Assess for Plasmodium parasites.
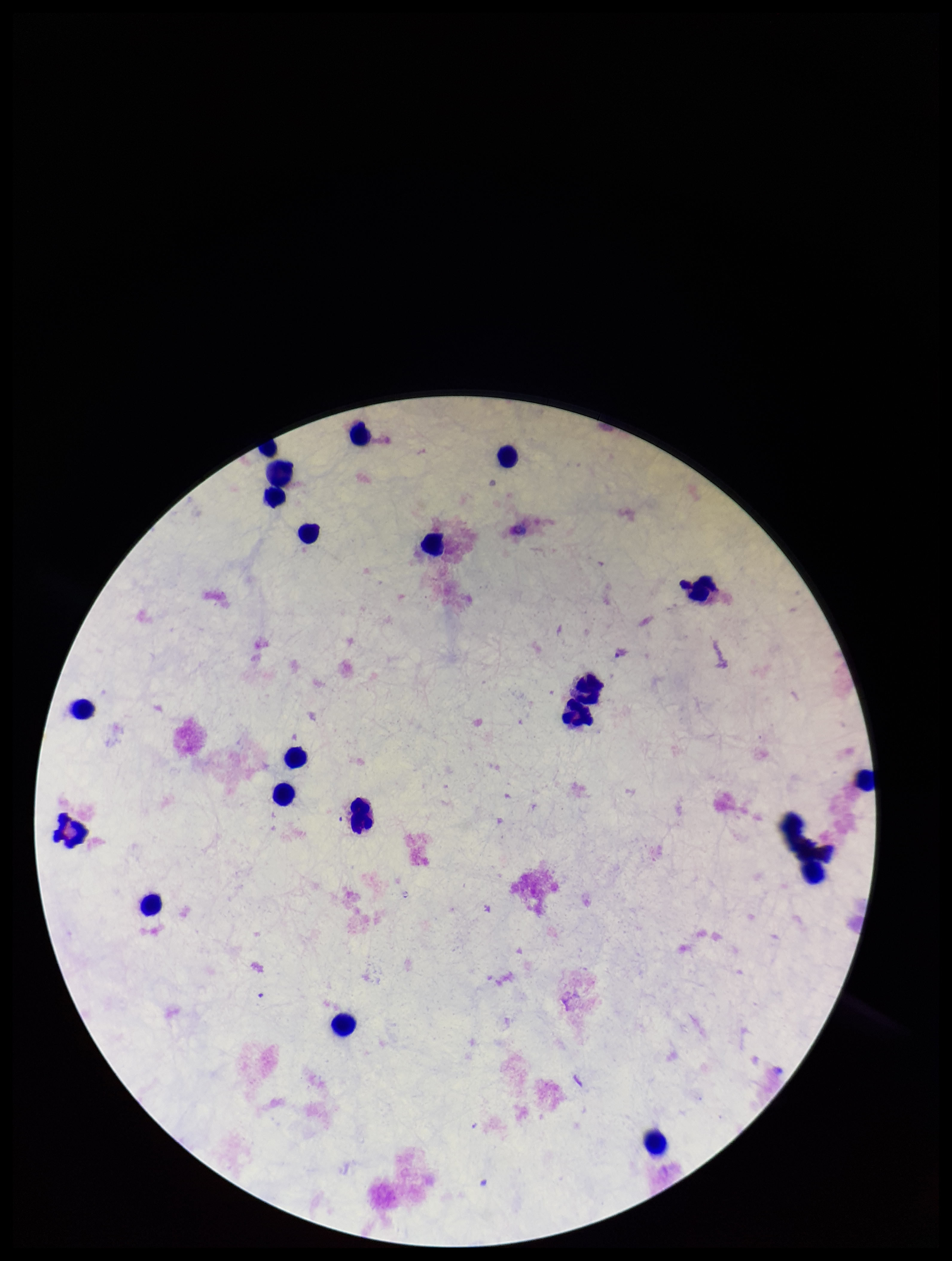

None seen.

Summary:
  - Field of view: one from this slide
  - Leukocyte count: 20
  - Stain: Giemsa
  - Image size: 952×1261 pixels
  - Patient malaria status: negative
  - Preparation: thick
  - Capture: smartphone photograph through the microscope eyepiece
  - Parasite count: 0